Identify the parasite.
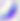

This is Toxoplasma gondii.

Summary:
  - Modality: micrograph
  - Magnification: 400x